Name the cell type shown.
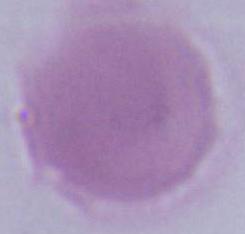

This is an erythrocyte.

magnification = 1000x
modality = photomicrograph